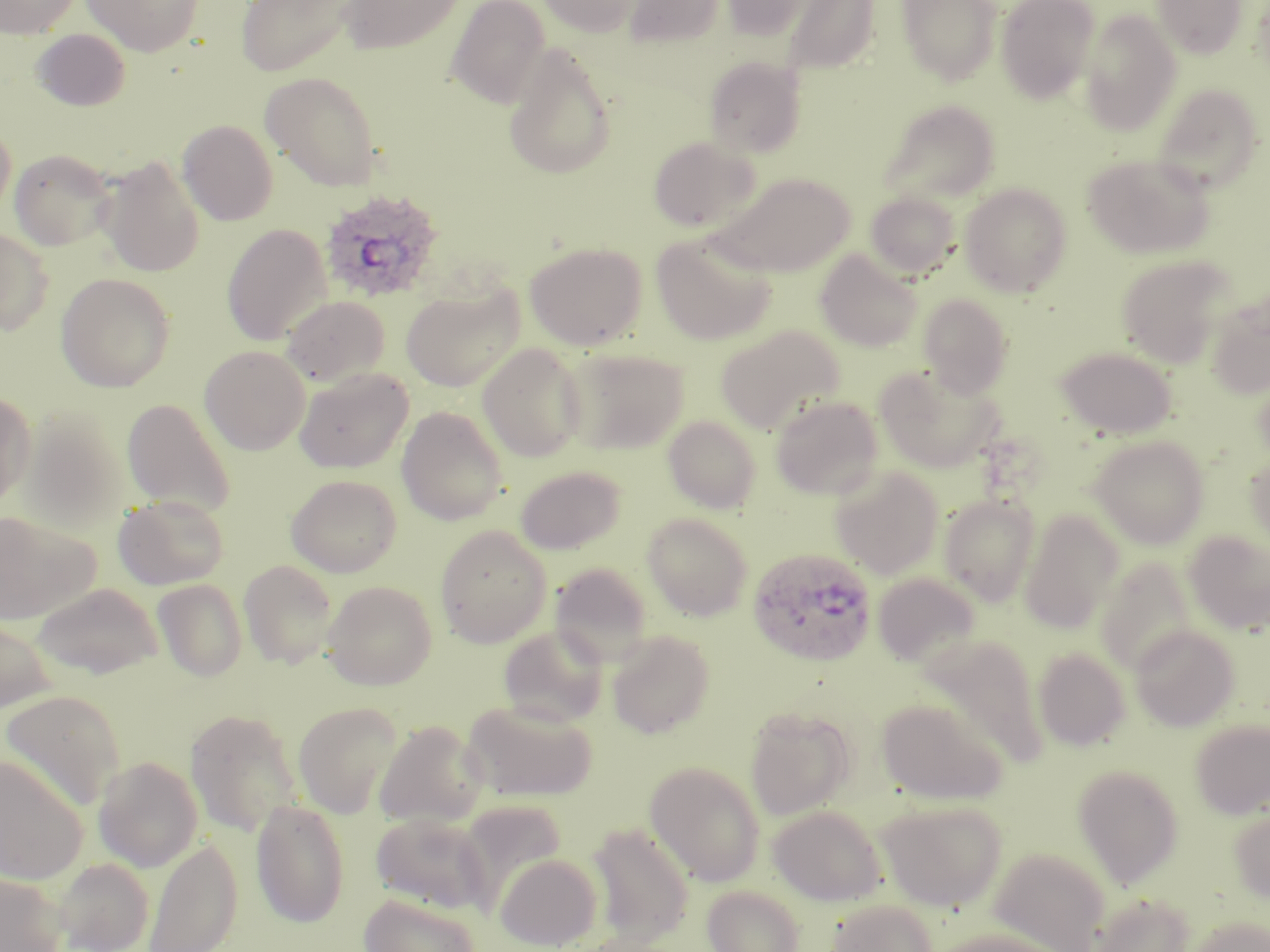
Approximate bounding boxes as (x1,y1)-(x2,y2) corner pairs in pixels. Plasmodium ovale-infected red blood cell locations: (319,187)-(444,304), (748,547)-(877,666). Uninfected red blood cell locations: (0,0)-(82,38), (81,0)-(203,57), (236,0)-(360,78), (338,0)-(466,55), (446,0)-(552,109), (536,0)-(644,37), (623,0)-(726,48), (718,0)-(820,41), (782,0)-(880,76), (896,0)-(1002,85), (996,0)-(1100,103), (1153,0)-(1246,58), (1079,8)-(1182,136), (32,29)-(131,111), (503,44)-(618,180), (703,56)-(808,158), (260,71)-(383,191), (1152,83)-(1264,191), (880,99)-(1000,206), (0,119)-(17,223), (178,119)-(279,226), (648,135)-(760,232), (9,148)-(118,251), (1083,153)-(1215,259), (98,157)-(204,277), (710,171)-(854,276), (959,182)-(1072,297), (864,191)-(961,280), (222,224)-(331,346), (0,228)-(54,335), (651,232)-(777,345), (525,241)-(647,350), (816,251)-(923,351), (1115,254)-(1237,367), (55,272)-(175,392), (402,283)-(523,393), (918,292)-(1014,398), (1206,292)-(1270,399), (281,295)-(390,387), (715,324)-(844,434), (478,343)-(588,462), (560,345)-(689,454), (199,346)-(310,455), (1055,346)-(1176,439), (294,366)-(413,473), (875,366)-(1003,474), (0,391)-(36,509), (770,394)-(885,500), (121,397)-(237,517), (396,406)-(508,525), (19,411)-(133,533), (663,415)-(762,514), (1089,435)-(1209,548), (1245,453)-(1270,550), (515,465)-(626,554), (829,465)-(943,578), (286,474)-(402,577), (940,493)-(1040,605), (113,494)-(230,590), (0,510)-(99,625), (1020,510)-(1124,633), (642,512)-(754,621), (435,525)-(553,647), (1183,530)-(1270,635), (1094,557)-(1199,676), (239,560)-(338,668), (549,562)-(655,666), (872,571)-(981,669), (152,578)-(248,682), (322,580)-(437,690), (32,582)-(164,679), (0,613)-(56,714), (1130,624)-(1240,731), (497,625)-(609,727), (607,630)-(715,738), (918,635)-(1049,768), (1033,647)-(1131,751), (1,691)-(125,809), (877,697)-(1007,805), (462,699)-(598,801), (293,702)-(403,818), (744,707)-(856,820), (185,709)-(304,836), (1190,718)-(1269,819), (373,720)-(487,828), (0,753)-(88,885), (93,756)-(203,871), (644,760)-(766,886), (1073,764)-(1184,888), (251,798)-(350,927), (877,799)-(1007,911), (768,804)-(887,906), (463,805)-(571,913), (1228,808)-(1270,903), (370,812)-(492,913), (587,823)-(695,947), (143,837)-(243,952), (990,848)-(1110,951), (495,853)-(602,950), (53,856)-(155,952), (0,870)-(69,952), (702,884)-(805,952), (1089,892)-(1196,952), (359,893)-(482,952), (825,897)-(939,952), (1187,914)-(1269,952), (931,928)-(1066,952). Slide-level diagnosis: Plasmodium ovale. Thin blood smear. Image is 1270×952 pixels. Light microscopy. 1000x magnification. May-Grünwald-Giemsa-stained preparation. One field of a larger specimen.